Point out each Plasmodium parasite.
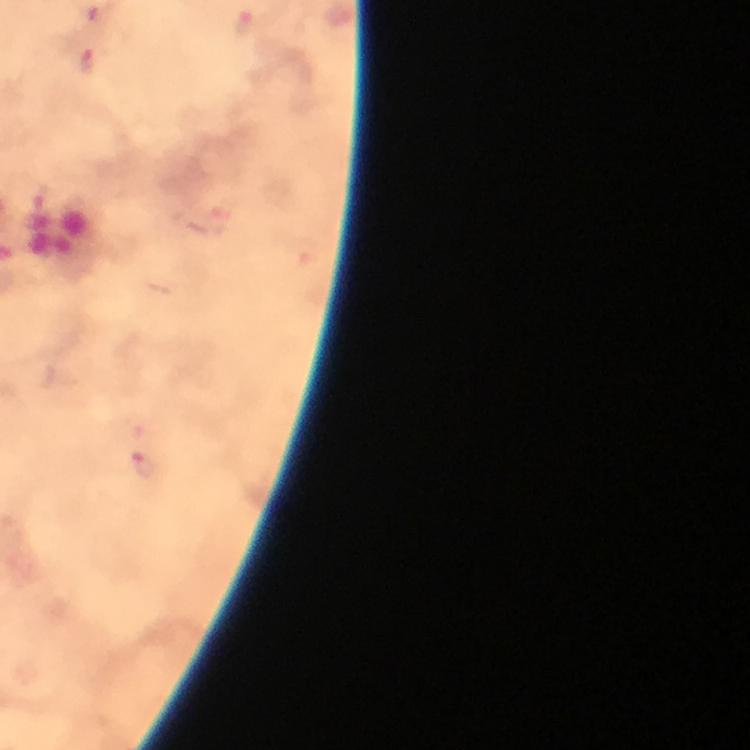
Approximate centers as [x, y] in pixels.
Plasmodium parasites: [244, 22], [87, 61], [145, 464].

{
  "context": "from a diagnostic examination for malaria",
  "magnification": "100x",
  "stain": "Giemsa",
  "capture": "smartphone photograph through a microscope",
  "preparation": "thick blood smear",
  "image_size": "750×750 pixels",
  "immersion_oil": "used",
  "cropped_from": "one field of view"
}